Give the extent of all uninfected red blood cells.
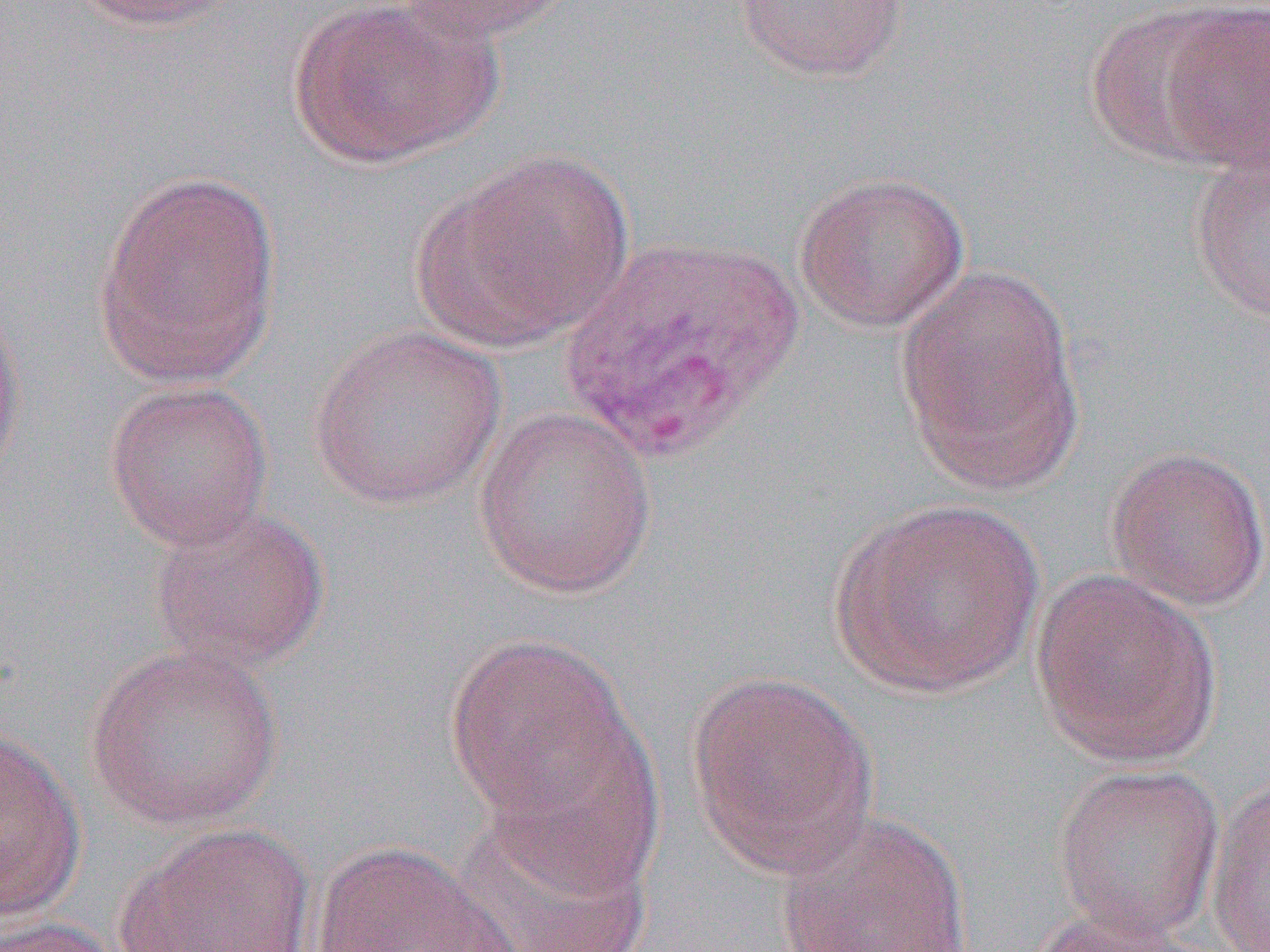
Approximate bounding boxes as (x1,y1)-(x2,y2) corner pairs in pixels.
Uninfected red blood cells: (70,0)-(253,33), (285,0)-(498,167), (389,0)-(577,44), (733,0)-(910,83), (1156,1)-(1270,173), (1083,4)-(1241,166), (425,149)-(634,348), (1188,152)-(1270,324), (90,169)-(283,387), (793,169)-(971,332), (893,264)-(1083,489), (0,294)-(27,491), (307,323)-(506,511), (103,380)-(273,551), (472,406)-(656,599), (1104,444)-(1270,612), (828,498)-(1044,699), (146,503)-(332,674), (1031,569)-(1222,767), (442,633)-(634,824), (84,642)-(285,830), (685,669)-(880,875), (480,720)-(665,899), (0,728)-(86,922), (1051,762)-(1225,941), (1205,775)-(1269,951), (452,805)-(658,951), (773,808)-(977,952), (112,822)-(316,952), (310,840)-(520,951), (1021,905)-(1206,952), (0,915)-(127,952).

Summary:
  - Slide-level diagnosis: Plasmodium vivax
  - Preparation: thin blood smear
  - Image size: 1270×952 pixels
  - Modality: light microscopy
  - Magnification: 1000x
  - Field of view: one of a larger specimen